Identify the parasite.
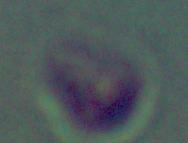

This is Leishmania.

Photomicrograph. Captured at 1000x magnification.